Locate every malaria parasite.
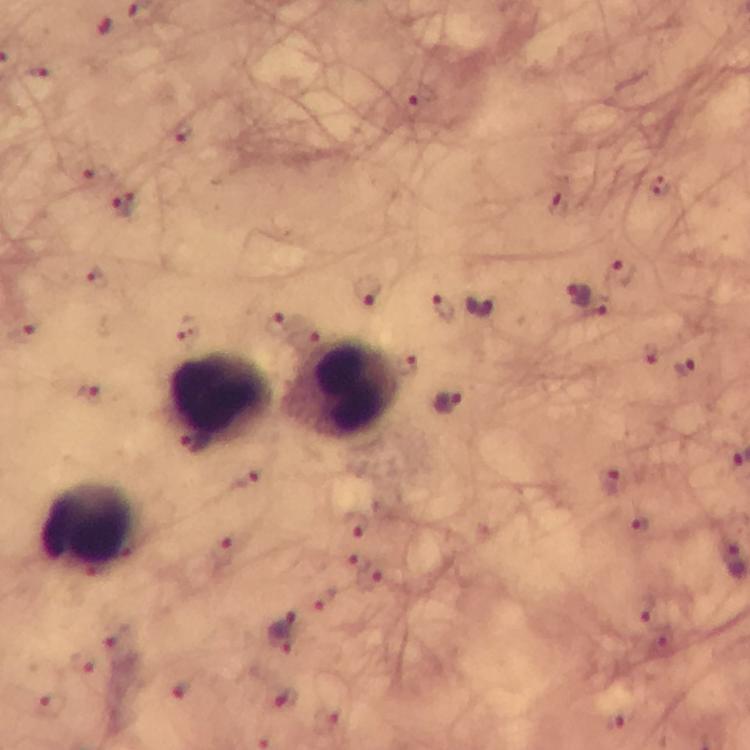

Approximate object centers, in pixels from the top-left corner.
Malaria parasites: (x=38, y=72), (x=421, y=96), (x=124, y=204), (x=559, y=204), (x=623, y=271), (x=98, y=280), (x=367, y=290), (x=579, y=295), (x=444, y=307), (x=480, y=307), (x=273, y=323), (x=652, y=357), (x=407, y=364), (x=685, y=370), (x=88, y=394), (x=448, y=403), (x=195, y=442), (x=248, y=480), (x=611, y=481), (x=355, y=525), (x=642, y=525), (x=224, y=550), (x=367, y=577), (x=645, y=609), (x=283, y=631), (x=116, y=634), (x=79, y=661), (x=181, y=689), (x=285, y=701), (x=50, y=706), (x=614, y=721), (x=324, y=724).

Summary:
  - Leukocyte locations: (x=343, y=388), (x=222, y=401), (x=89, y=526)
  - Stain: Giemsa
  - Cropped from: a single field of view
  - Preparation: thick smear
  - Context: from a diagnostic examination for malaria
  - Magnification: 100x
  - Immersion oil: applied
  - Image size: 750×750 pixels
  - Capture: smartphone camera through the microscope